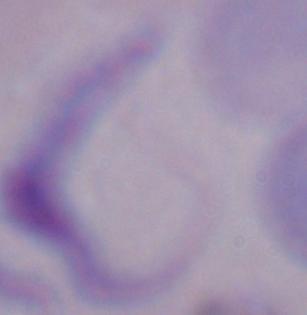

1000x magnification. Photomicrograph. A trypanosome is seen.